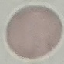
Malaria status: uninfected. Giemsa stain. Automatically extracted cell patch, resized to 64 × 64 pixels. Acquired by smartphone through the microscope eyepiece. Thin blood smear.